Identify the parasite.
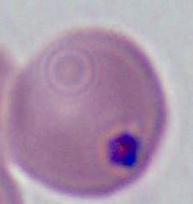
Plasmodium.

400x or 1000x magnification. Micrograph.